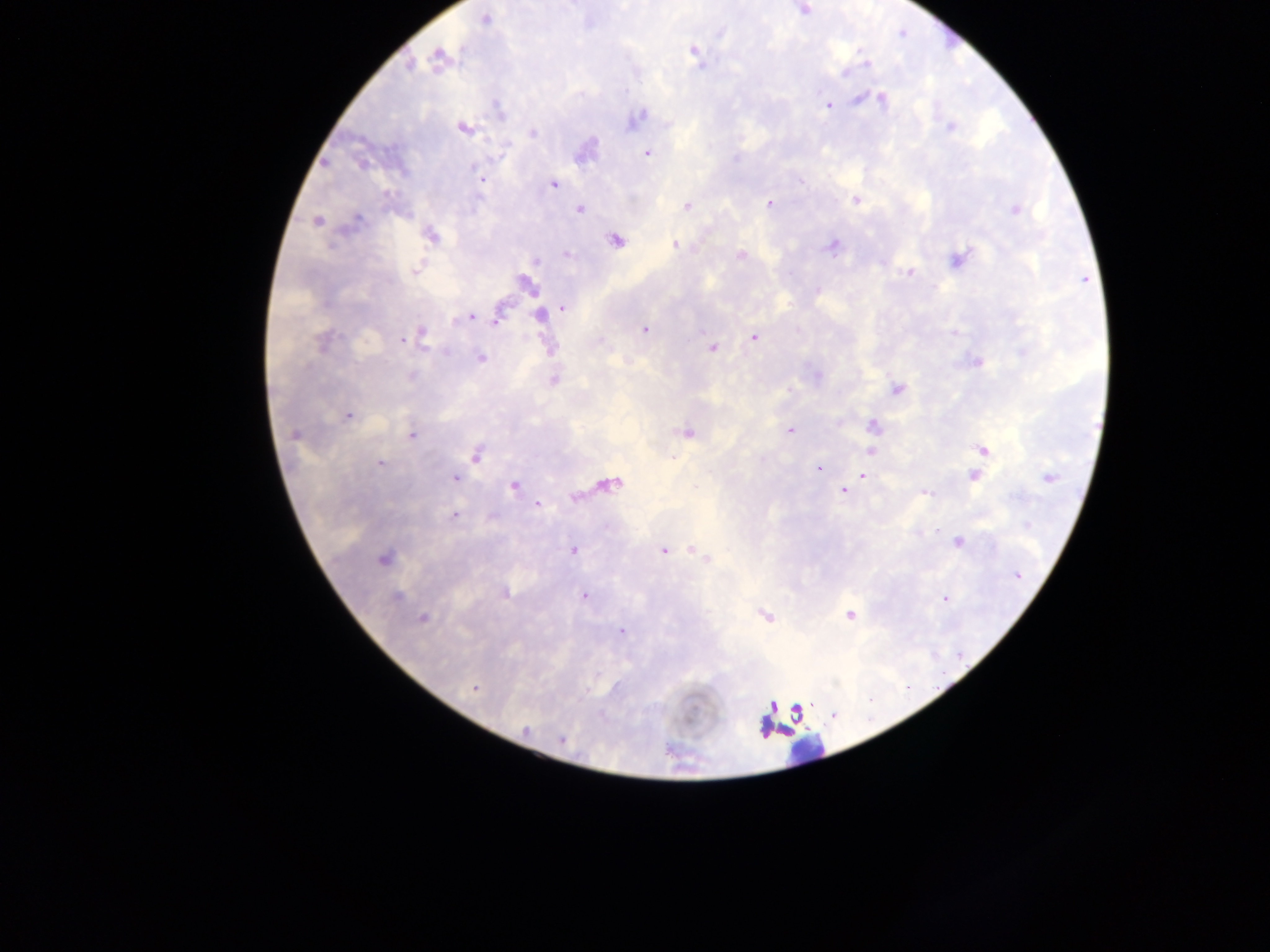
Approximate centers as (x, y) in pixels. Leukocyte locations: (809, 753). Malaria parasite locations: (804, 10), (486, 20), (693, 52), (438, 57), (866, 63), (409, 65), (844, 73), (859, 98), (883, 99), (827, 104), (499, 110), (637, 119), (950, 127), (464, 128), (533, 133), (647, 153), (735, 159), (475, 168), (477, 174), (480, 180), (554, 185), (856, 200), (769, 204), (686, 207), (579, 210), (1014, 210), (358, 220), (316, 222), (431, 237), (615, 241), (675, 245), (832, 247), (567, 254), (740, 256), (957, 258), (537, 261), (416, 270), (908, 273), (527, 285), (817, 291), (564, 308), (540, 315), (469, 317), (498, 319), (644, 330), (422, 334), (754, 337), (402, 341), (599, 341), (321, 343), (712, 349), (480, 358), (976, 363), (412, 377), (554, 380), (896, 389), (348, 415), (873, 426), (790, 431), (687, 432), (294, 435), (412, 435), (983, 449), (870, 451), (476, 456), (674, 458), (380, 463), (818, 468), (972, 475), (864, 476), (1048, 478), (455, 479), (611, 484), (514, 486), (844, 491), (926, 493), (575, 497), (538, 505), (454, 515), (493, 517), (958, 542), (574, 550), (663, 550), (697, 553), (703, 557), (382, 559), (1017, 576), (504, 593), (396, 596), (584, 596), (945, 598), (766, 615), (850, 615), (422, 618), (622, 631), (474, 689), (772, 705), (797, 712), (525, 731), (562, 739). Collected in Ghana. One field of view. Mobile-phone photograph taken through the microscope. Thick blood film. Image is 1270×952 pixels.